Identify the parasite.
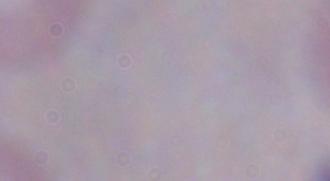
A trypanosome.

magnification = 1000x
modality = micrograph